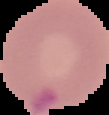

Summary:
  - Image size: 109×115 pixels
  - Preparation: thin blood film
  - Malaria status: parasitized
  - Image type: segmented cell region on a black background